Give the location of every parasitized red blood cell.
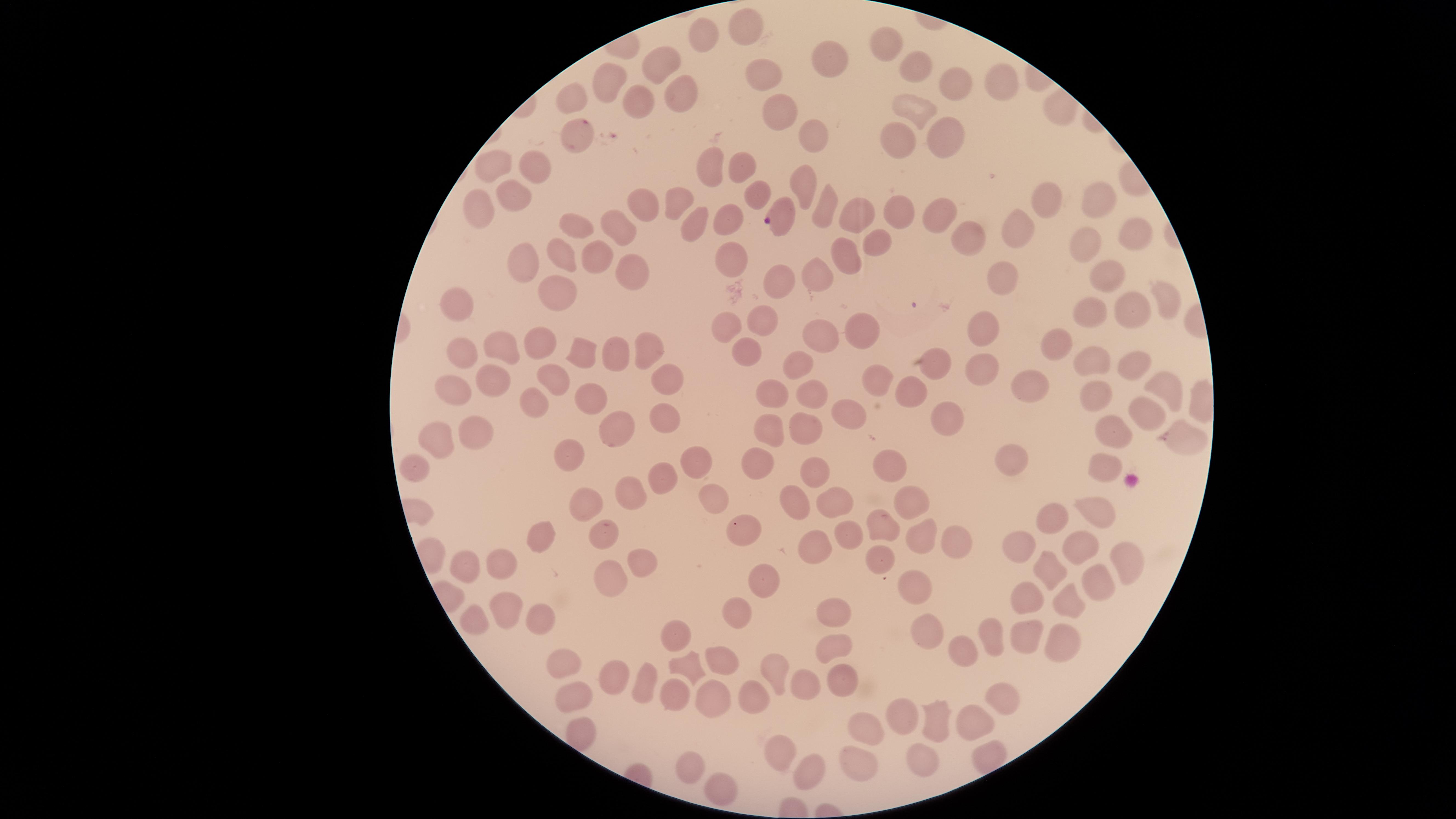

No parasitized red blood cells identified.

stain = Giemsa
visible region = circular
field of view = single
uninfected red blood cells = approximate marker points, in pixels from the top-left corner: (x=744, y=25), (x=712, y=38), (x=889, y=44), (x=668, y=58), (x=836, y=62), (x=920, y=70), (x=756, y=72), (x=614, y=82), (x=1006, y=83), (x=946, y=86), (x=682, y=94), (x=645, y=98), (x=576, y=99), (x=909, y=107), (x=782, y=113), (x=814, y=132), (x=577, y=137), (x=943, y=137), (x=894, y=138), (x=708, y=163), (x=737, y=167), (x=500, y=168), (x=534, y=170), (x=804, y=186), (x=753, y=188), (x=511, y=191), (x=672, y=197), (x=1100, y=199), (x=647, y=202), (x=1045, y=202), (x=823, y=204), (x=472, y=211), (x=848, y=211), (x=726, y=216), (x=899, y=216), (x=945, y=218), (x=692, y=219), (x=582, y=226), (x=1012, y=226), (x=621, y=228), (x=1134, y=232), (x=974, y=238), (x=874, y=239), (x=1086, y=249), (x=569, y=254), (x=602, y=257), (x=730, y=258), (x=849, y=258), (x=628, y=264), (x=528, y=265), (x=1100, y=273), (x=1004, y=275), (x=814, y=276), (x=775, y=279), (x=557, y=289), (x=1162, y=296), (x=459, y=303), (x=1095, y=311), (x=1133, y=312), (x=768, y=318), (x=984, y=324), (x=732, y=327), (x=861, y=335), (x=825, y=336), (x=546, y=343), (x=1056, y=344), (x=653, y=346), (x=752, y=348), (x=619, y=349), (x=500, y=350), (x=588, y=355), (x=459, y=356), (x=798, y=359), (x=1130, y=360), (x=1089, y=364), (x=938, y=366), (x=980, y=370), (x=869, y=375), (x=1025, y=378), (x=493, y=380), (x=557, y=380), (x=666, y=380), (x=1165, y=386), (x=454, y=389), (x=771, y=389), (x=912, y=393), (x=589, y=395), (x=815, y=395), (x=1100, y=395), (x=530, y=401), (x=1144, y=406), (x=848, y=411), (x=666, y=418), (x=943, y=418), (x=607, y=429), (x=480, y=431), (x=771, y=432), (x=1123, y=436), (x=441, y=437), (x=1179, y=437), (x=815, y=439), (x=575, y=451), (x=1011, y=457), (x=885, y=460), (x=419, y=462), (x=703, y=462), (x=760, y=463), (x=1105, y=463), (x=803, y=466), (x=660, y=475), (x=793, y=489), (x=633, y=490), (x=712, y=492), (x=904, y=497), (x=582, y=503), (x=845, y=503), (x=1089, y=505), (x=1049, y=517), (x=878, y=520), (x=599, y=525), (x=740, y=526), (x=843, y=531), (x=913, y=532), (x=539, y=537), (x=954, y=541), (x=815, y=542), (x=1018, y=545), (x=1082, y=545), (x=635, y=557), (x=1122, y=557), (x=880, y=559), (x=469, y=561), (x=500, y=561), (x=763, y=571), (x=1058, y=574), (x=1098, y=579), (x=616, y=581), (x=910, y=583), (x=1035, y=594), (x=1066, y=598), (x=501, y=604), (x=827, y=609), (x=741, y=612), (x=537, y=616), (x=477, y=625), (x=677, y=634), (x=923, y=636), (x=1020, y=636), (x=993, y=637), (x=1053, y=641), (x=839, y=645), (x=972, y=657), (x=689, y=658), (x=726, y=660), (x=563, y=663), (x=778, y=671), (x=615, y=675), (x=839, y=676), (x=644, y=680), (x=800, y=682), (x=575, y=687), (x=675, y=690), (x=759, y=694), (x=996, y=696), (x=707, y=698), (x=966, y=718), (x=905, y=721), (x=936, y=721), (x=861, y=728), (x=772, y=746), (x=925, y=758), (x=687, y=764), (x=860, y=767), (x=805, y=771), (x=720, y=790)
preparation = thin smear of blood
capture = smartphone photograph through the microscope eyepiece
image size = 1456×819 pixels